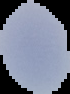
Summary:
  - Image type: segmented cell region on a black background
  - Malaria status: uninfected
  - Image size: 70×94 pixels
  - Preparation: thin blood film